Comment on the morphology of the red blood cells.
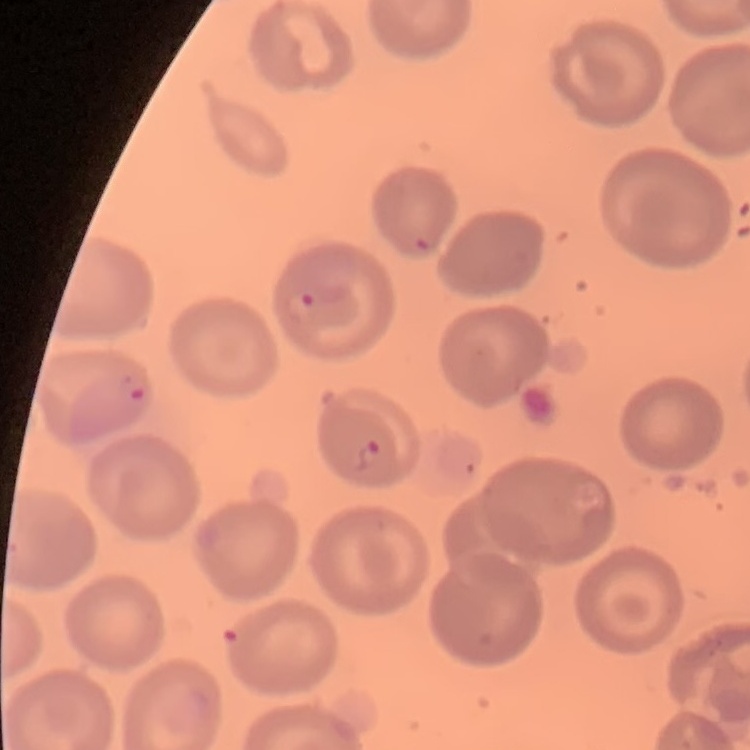

They show no rouleaux formation.

Square crop of a larger photomicrograph. Thin blood film. Stained with either Field's or Giemsa.